Point out each malaria parasite and classify it by life-cycle stage.
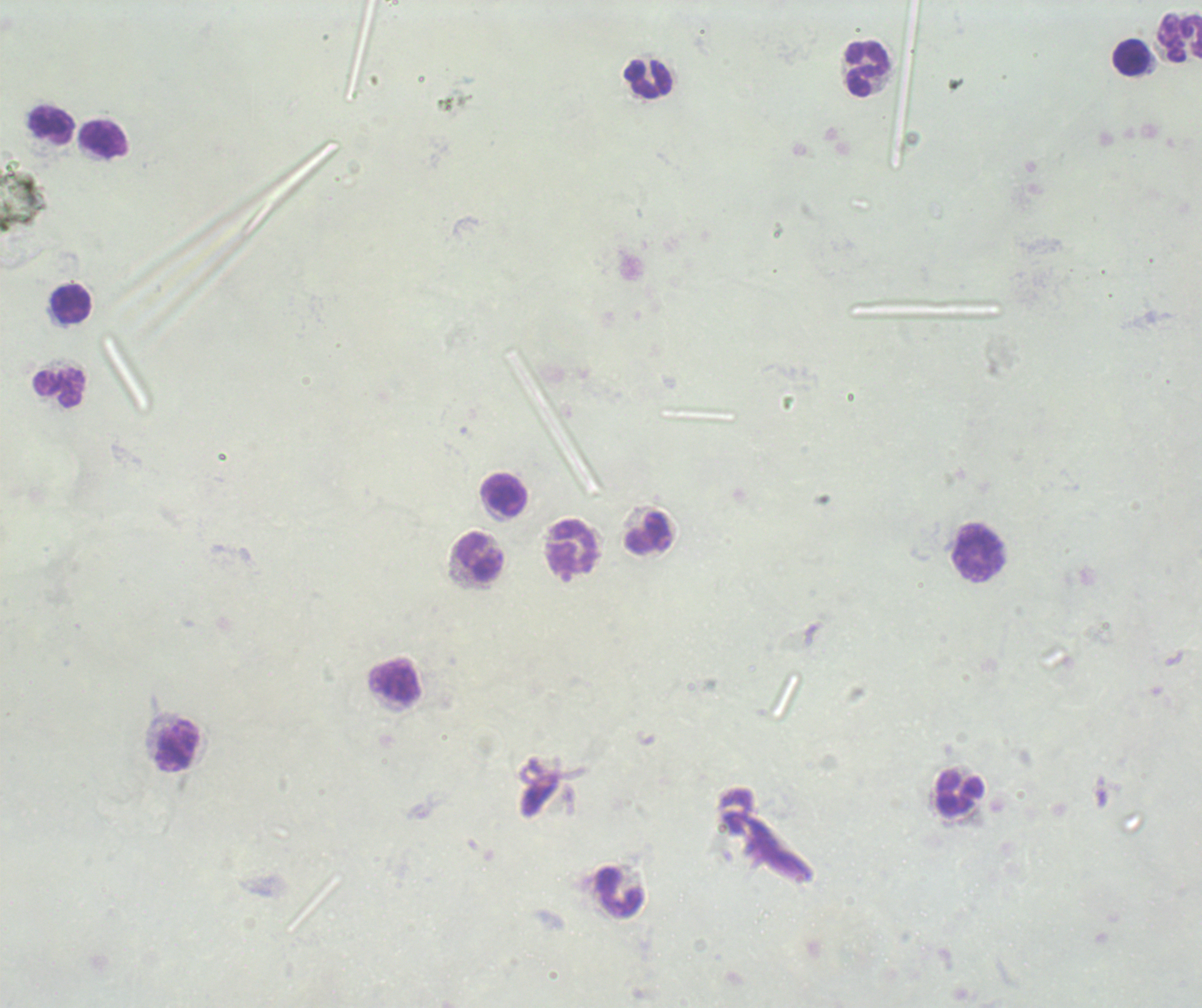
Negative for malaria parasites.

field_of_view: one from this slide
image_size: 1202×1008 pixels
stain: Romanowsky
context: previously used in a real diagnosis
magnification: 100x
preparation: thick blood film
leukocyte_locations: 'approximate centers as [x, y] in pixels: [1179, 38], [1132, 57], [867, 69], [649, 78], [52, 126], [104, 141], [72, 303], [59, 388], [504, 496], [648, 534], [574, 549], [978, 554], [480, 557], [394, 681], [177, 747], [960, 794], [620, 893]'
background_quality: unsatisfactory